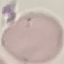 Malaria status: uninfected. Giemsa-stained preparation. Photographed with a smartphone camera at the microscope eyepiece. Thin smear of blood. Automatically extracted cell patch, resized to 64 × 64 pixels.